Identify the parasite.
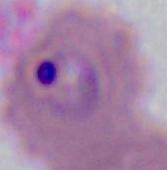

This is Plasmodium.

magnification = 400x or 1000x
modality = photomicrograph